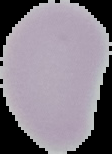

Segmented cell region on a black background. Image is 112×154 pixels. From a thin blood smear. Result: no malaria parasites seen.